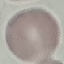

Summary:
  - Malaria status: uninfected
  - Capture: smartphone camera at the microscope eyepiece
  - Image type: automatically extracted cell patch, resized to 64 × 64 pixels
  - Preparation: thin blood smear
  - Stain: Giemsa